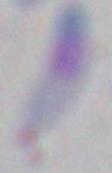
Photomicrograph. 1000x magnification. Toxoplasma gondii is shown.